State which parasite is depicted.
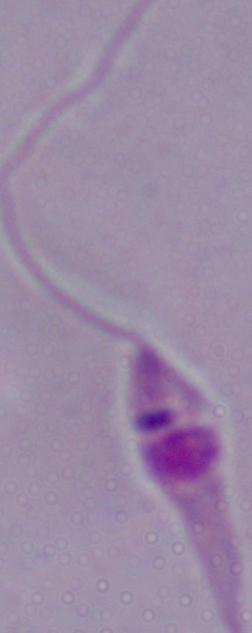
This is Leishmania.

modality = micrograph
magnification = 1000x